Locate every uninfected red blood cell.
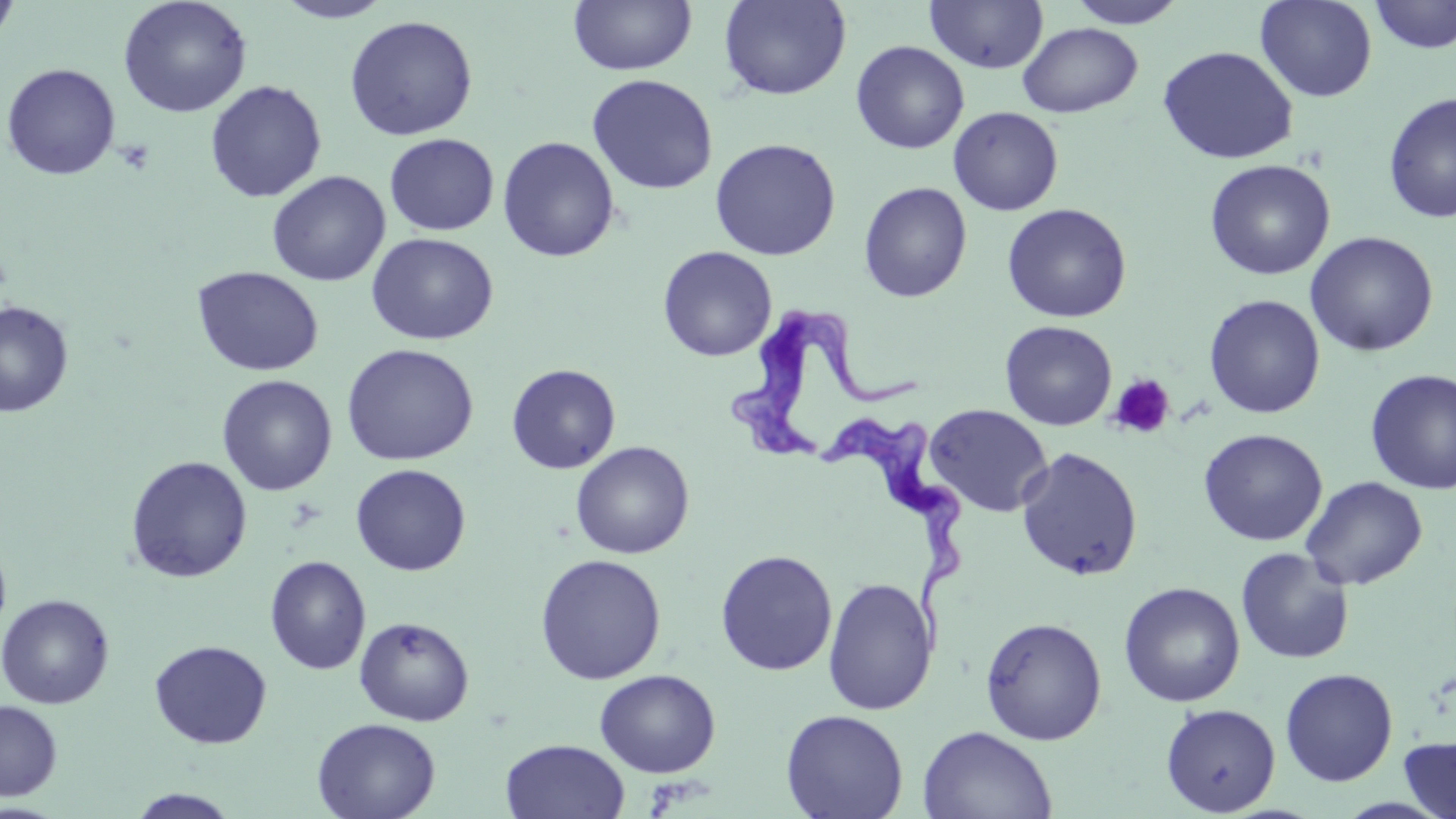

Approximate bounding boxes as named x1/y1/x2/y2 corners in pixels.
Uninfected red blood cells: (x1=0, y1=0, x2=20, y2=51), (x1=117, y1=0, x2=252, y2=118), (x1=273, y1=0, x2=395, y2=23), (x1=568, y1=0, x2=697, y2=76), (x1=718, y1=0, x2=851, y2=100), (x1=925, y1=0, x2=1049, y2=74), (x1=1066, y1=0, x2=1189, y2=28), (x1=1255, y1=0, x2=1378, y2=103), (x1=1368, y1=0, x2=1456, y2=54), (x1=344, y1=14, x2=479, y2=141), (x1=1017, y1=22, x2=1143, y2=117), (x1=851, y1=40, x2=969, y2=154), (x1=1157, y1=45, x2=1299, y2=164), (x1=1, y1=63, x2=121, y2=181), (x1=585, y1=74, x2=719, y2=195), (x1=205, y1=80, x2=327, y2=202), (x1=1383, y1=92, x2=1456, y2=223), (x1=948, y1=106, x2=1063, y2=216), (x1=384, y1=134, x2=499, y2=236), (x1=497, y1=135, x2=620, y2=262), (x1=709, y1=138, x2=841, y2=261), (x1=1204, y1=159, x2=1336, y2=280), (x1=267, y1=171, x2=391, y2=287), (x1=858, y1=181, x2=973, y2=303), (x1=1002, y1=203, x2=1132, y2=323), (x1=1304, y1=231, x2=1439, y2=357), (x1=366, y1=232, x2=499, y2=345), (x1=657, y1=246, x2=777, y2=362), (x1=192, y1=265, x2=324, y2=377), (x1=1204, y1=294, x2=1325, y2=419), (x1=0, y1=300, x2=74, y2=417), (x1=1000, y1=320, x2=1117, y2=431), (x1=341, y1=343, x2=479, y2=466), (x1=506, y1=363, x2=621, y2=474), (x1=1364, y1=368, x2=1456, y2=494), (x1=217, y1=374, x2=337, y2=496), (x1=925, y1=403, x2=1053, y2=517), (x1=1198, y1=428, x2=1328, y2=546), (x1=570, y1=441, x2=694, y2=559), (x1=1015, y1=446, x2=1144, y2=582), (x1=126, y1=455, x2=252, y2=583), (x1=350, y1=464, x2=471, y2=576), (x1=1300, y1=475, x2=1428, y2=590), (x1=0, y1=540, x2=12, y2=643), (x1=1236, y1=547, x2=1355, y2=665), (x1=715, y1=549, x2=837, y2=676), (x1=534, y1=553, x2=667, y2=685), (x1=264, y1=555, x2=371, y2=675), (x1=822, y1=576, x2=937, y2=715), (x1=1118, y1=581, x2=1246, y2=707), (x1=0, y1=593, x2=115, y2=709), (x1=354, y1=616, x2=474, y2=726), (x1=979, y1=616, x2=1107, y2=745), (x1=150, y1=640, x2=272, y2=749), (x1=1280, y1=667, x2=1399, y2=786), (x1=594, y1=669, x2=721, y2=777), (x1=0, y1=699, x2=62, y2=801), (x1=1160, y1=703, x2=1281, y2=816), (x1=780, y1=709, x2=909, y2=819), (x1=312, y1=716, x2=440, y2=819), (x1=918, y1=725, x2=1057, y2=819), (x1=1398, y1=733, x2=1456, y2=819), (x1=500, y1=738, x2=630, y2=819), (x1=126, y1=788, x2=242, y2=818).

slide_level_diagnosis: Trypanosoma brucei
image_size: 1456×819 pixels
field_of_view: single
modality: light microscopy
trypanosoma_brucei_locations: 'approximate bounding boxes as named x1/y1/x2/y2 corners in pixels: (x1=728, y1=300, x2=923, y2=469), (x1=816, y1=413, x2=970, y2=662)'
preparation: thin blood smear
platelet_locations: 'approximate bounding boxes as named x1/y1/x2/y2 corners in pixels: (x1=116, y1=139, x2=156, y2=174), (x1=1108, y1=374, x2=1176, y2=439)'
magnification: 1000x
stain: May-Grünwald-Giemsa